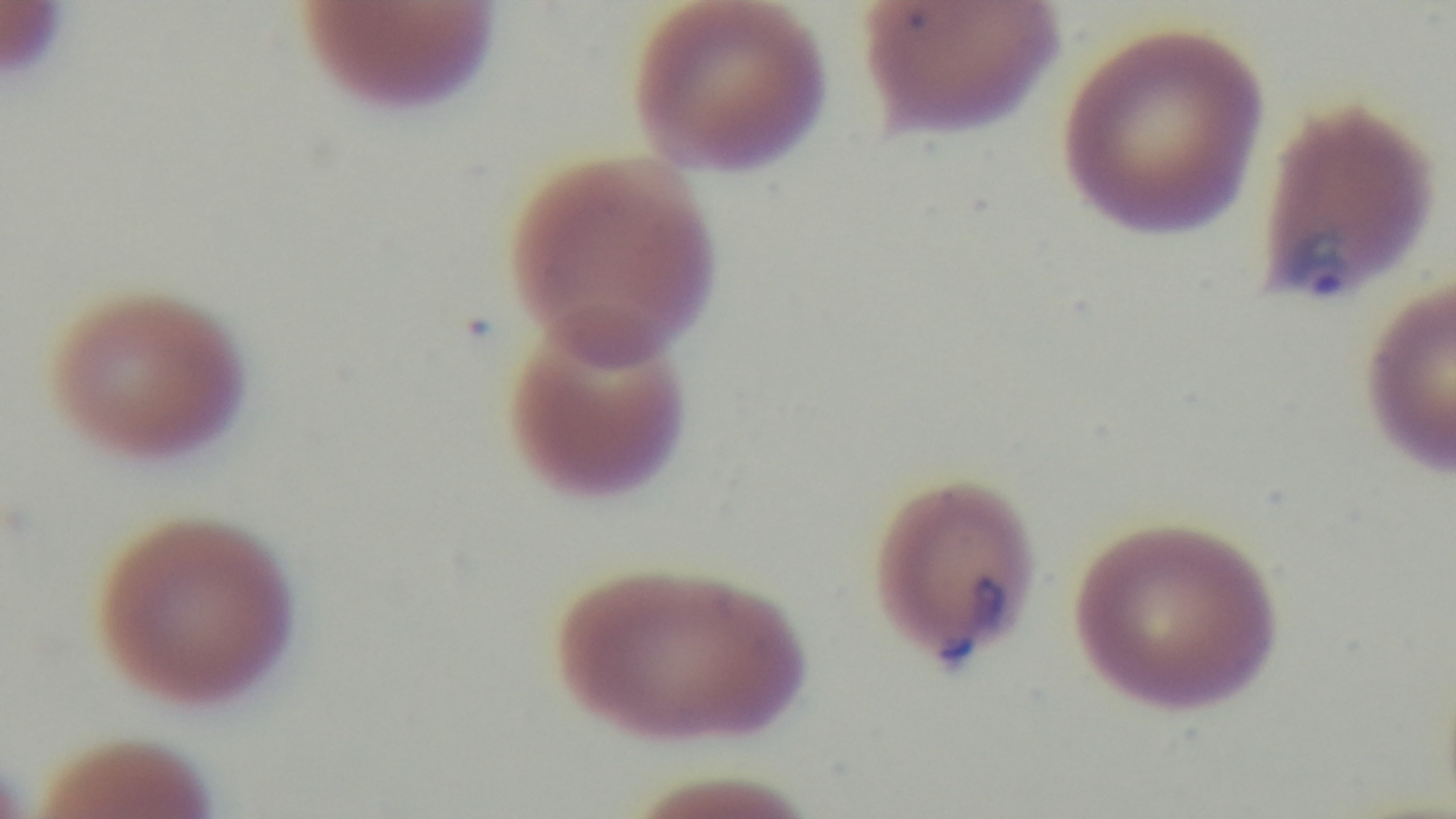

Malaria status: positive. Giemsa-stained. Captured with a mounted 4K digital camera. One field from the slide. Oil-immersion objective, 100x. Light microscopy. Preparation: thin smear.